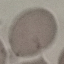

Summary:
  - Result: no malaria parasites seen
  - Preparation: thin smear
  - Stain: Giemsa
  - Capture: smartphone camera at the microscope eyepiece
  - Image type: cell patch, automatically extracted from a larger field of view and resized to 64 × 64 pixels